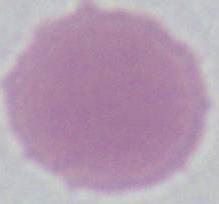
Summary:
  - Magnification: 1000x
  - Modality: micrograph
  - Identification: erythrocyte